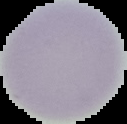

Image is 127×124 pixels. From a thin blood smear. Segmented cell region on a black background. Result: no malaria parasites seen.